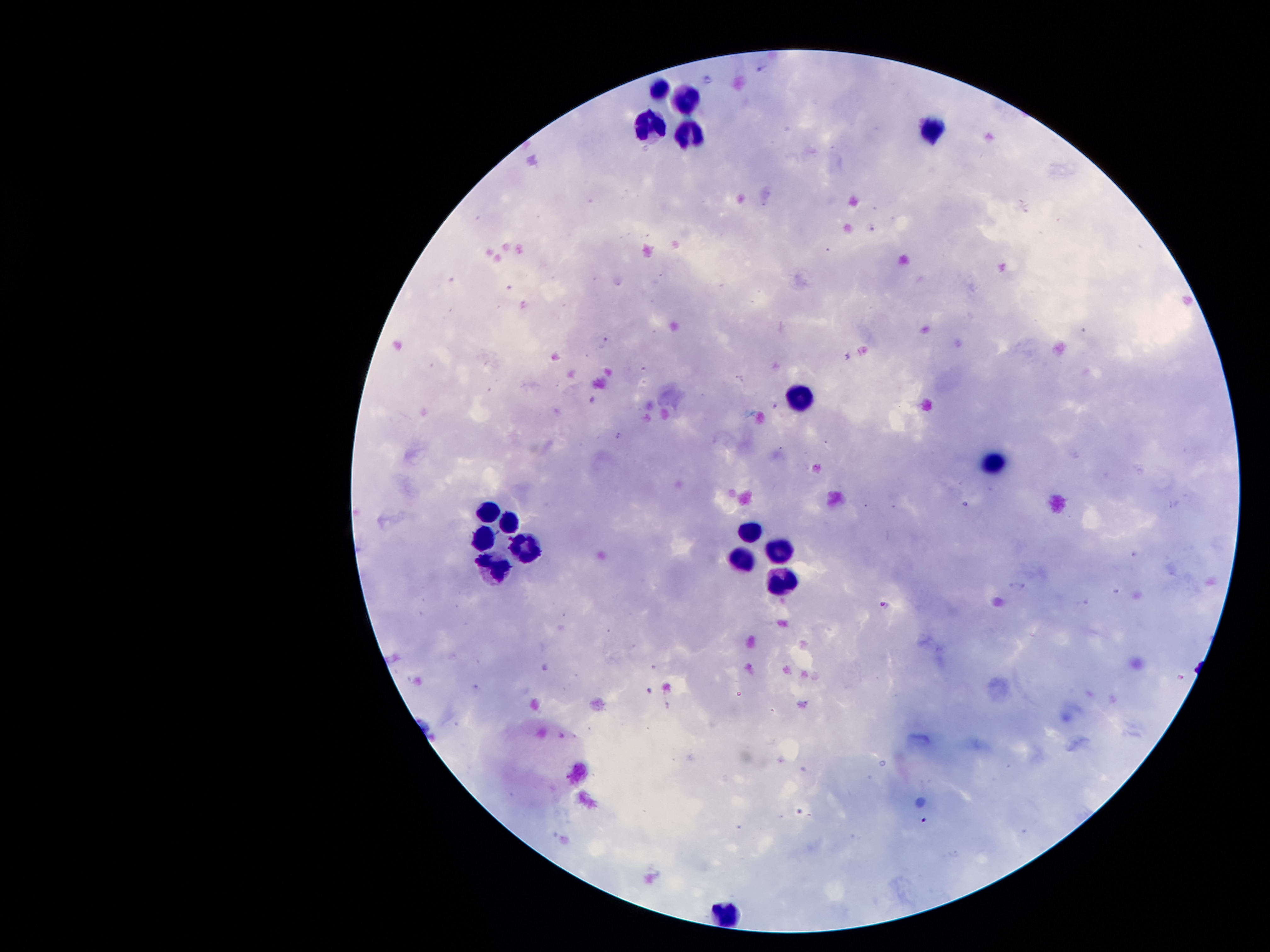
Approximate object centers, in pixels from the top-left corner.
Summary:
  - Leukocyte locations: (x=658, y=92), (x=687, y=95), (x=932, y=129), (x=654, y=131), (x=691, y=136), (x=803, y=400), (x=990, y=465), (x=486, y=510), (x=506, y=518), (x=746, y=531), (x=486, y=536), (x=523, y=549), (x=779, y=549), (x=746, y=559), (x=491, y=567), (x=782, y=580), (x=721, y=907)
  - Malaria parasite locations: (x=884, y=604), (x=649, y=689), (x=924, y=820)
  - Stain: Giemsa
  - Image size: 1270×952 pixels
  - Preparation: thick blood smear
  - Capture: smartphone through the microscope eyepiece
  - Magnification: 100x
  - Patient malaria status: positive for Plasmodium falciparum
  - Field of view: single